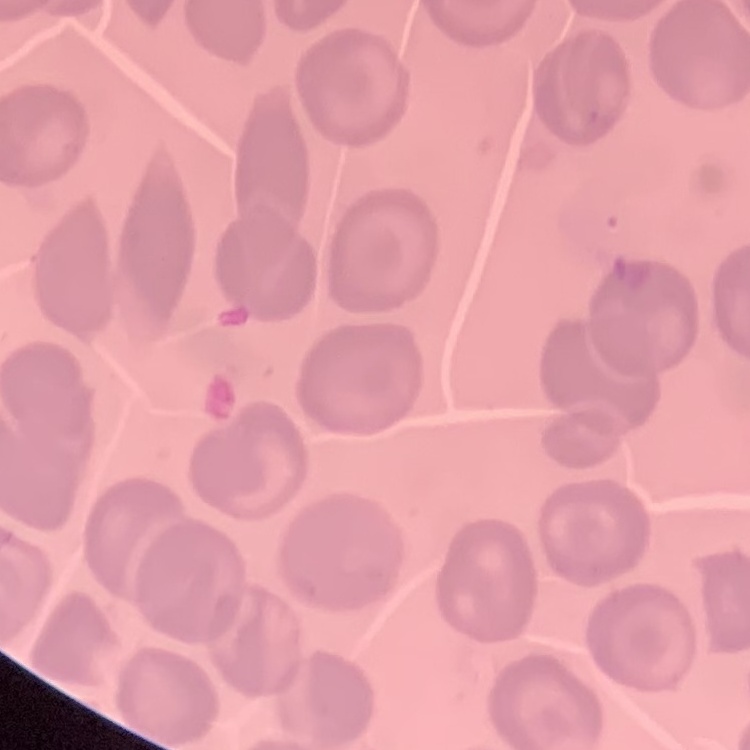
red_blood_cell_morphology: no rouleaux formation
preparation: thin blood film
image_type: one tile cut from a larger photomicrograph
stain: Field's or Giemsa